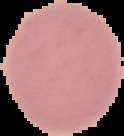
Summary:
  - Image type: cell region segmented out of the field of view; surrounding area masked to black
  - Image size: 124×136 pixels
  - Preparation: thin blood film
  - Result: no Plasmodium parasites seen